Locate malaria parasites and leukocytes.
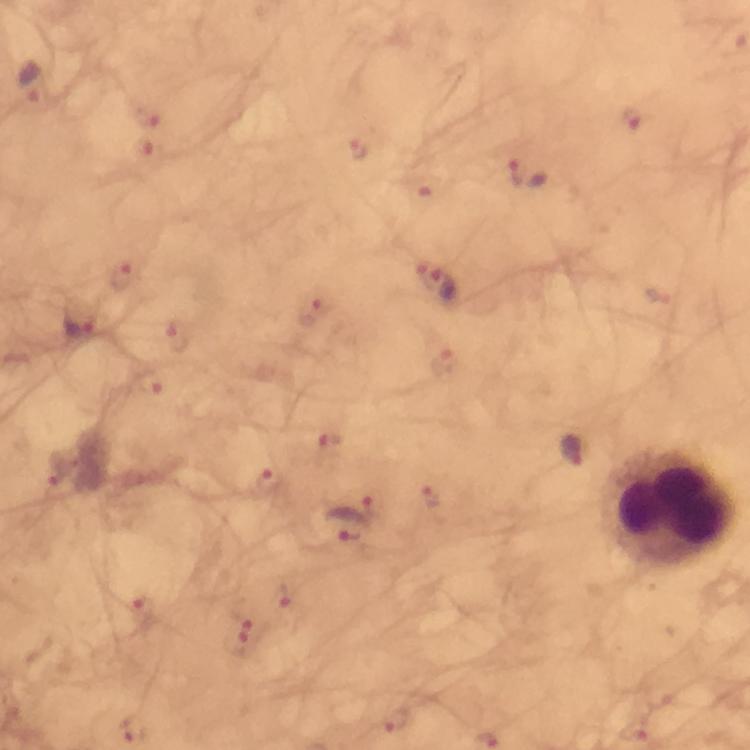
Approximate centers as (x, y) in pixels.
Malaria parasites: (30, 83), (147, 112), (633, 117), (361, 148), (515, 171), (124, 275), (436, 283), (313, 313), (78, 324), (179, 337), (444, 360), (152, 383), (329, 443), (57, 469), (268, 481), (433, 497), (370, 510), (342, 525), (284, 597), (141, 612), (244, 632), (397, 722).
Leukocytes: (668, 506).

{
  "magnification": "100x",
  "image_size": "750×750 pixels",
  "capture": "smartphone camera through the microscope",
  "context": "from a malaria diagnostic workup",
  "cropped_from": "a single field of view",
  "preparation": "thick blood smear",
  "stain": "Giemsa",
  "immersion_oil": "applied"
}